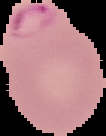

Result: Plasmodium parasites detected. From a thin blood film. Image is 106×136 pixels. Segmented cell region on a black background.